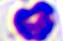
modality = micrograph
identification = white blood cell
magnification = 400x